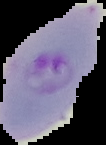

Segmented cell region on a black background. From a thin blood smear. Image is 106×145 pixels. Malaria status: parasitized.